Assess this cell for malaria.
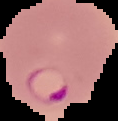

It is parasitized.

preparation = thin blood smear
image size = 118×121 pixels
image type = segmented cell region on a black background